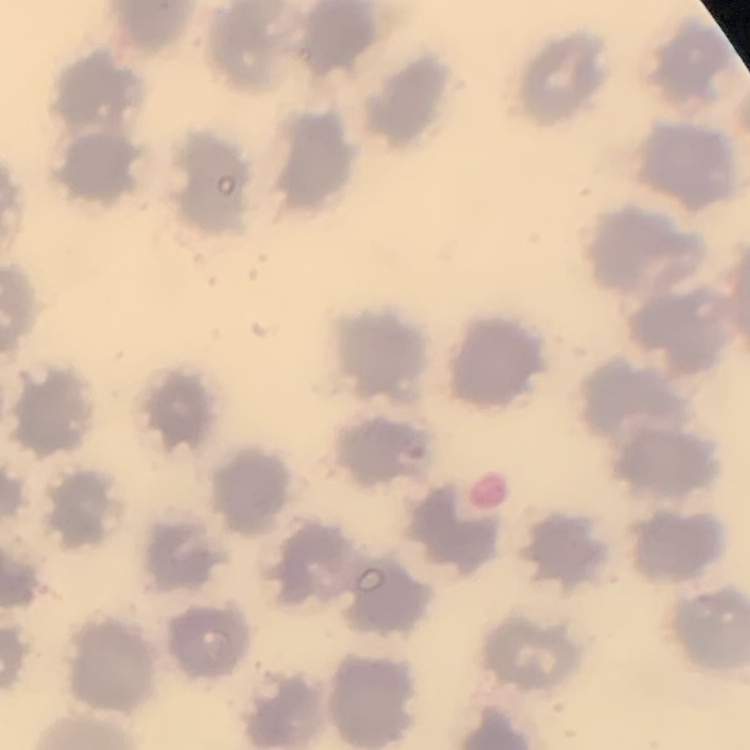

{
  "red_blood_cell_morphology": "no rouleaux formation",
  "preparation": "thin blood smear",
  "image_type": "square crop of a larger photomicrograph",
  "stain": "Field's or Giemsa"
}